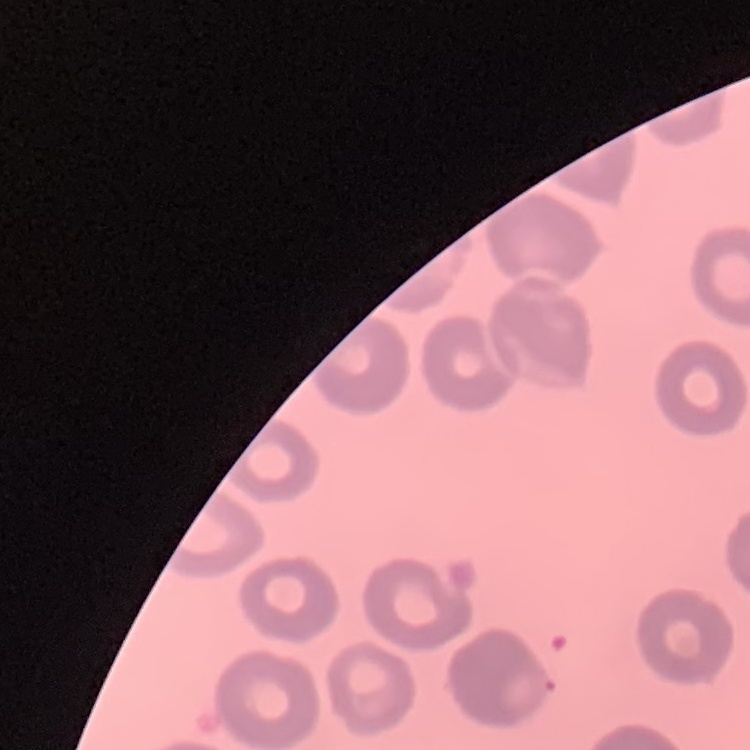 The erythrocytes exhibit no rouleaux formation. Thin blood smear. Field's or Giemsa stain. Square crop of a larger photomicrograph.